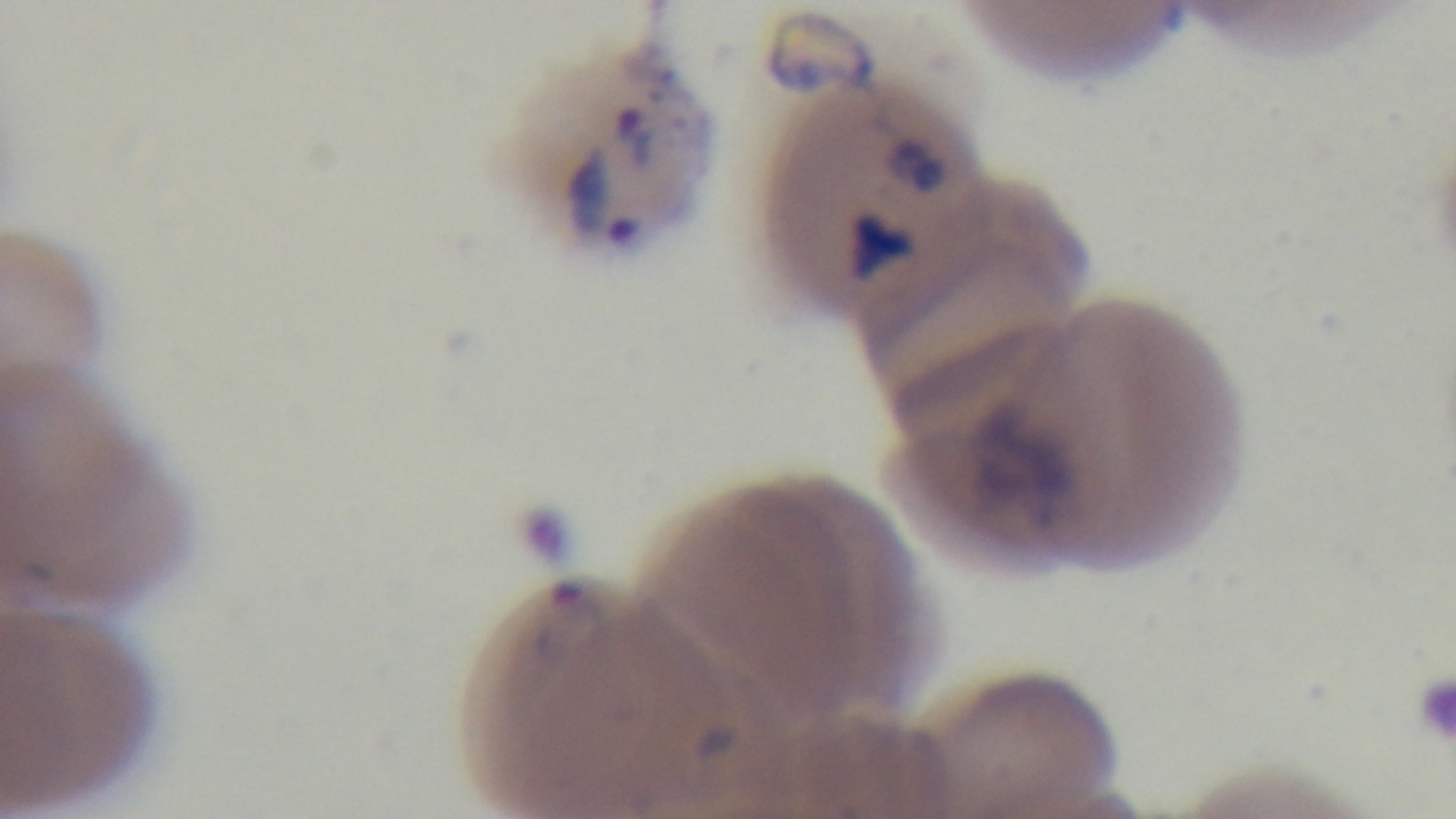
preparation = thin blood film
field of view = single
stain = Giemsa
capture = mounted 4K digital camera
modality = light microscopy
malaria status = infected
objective = 100x oil immersion